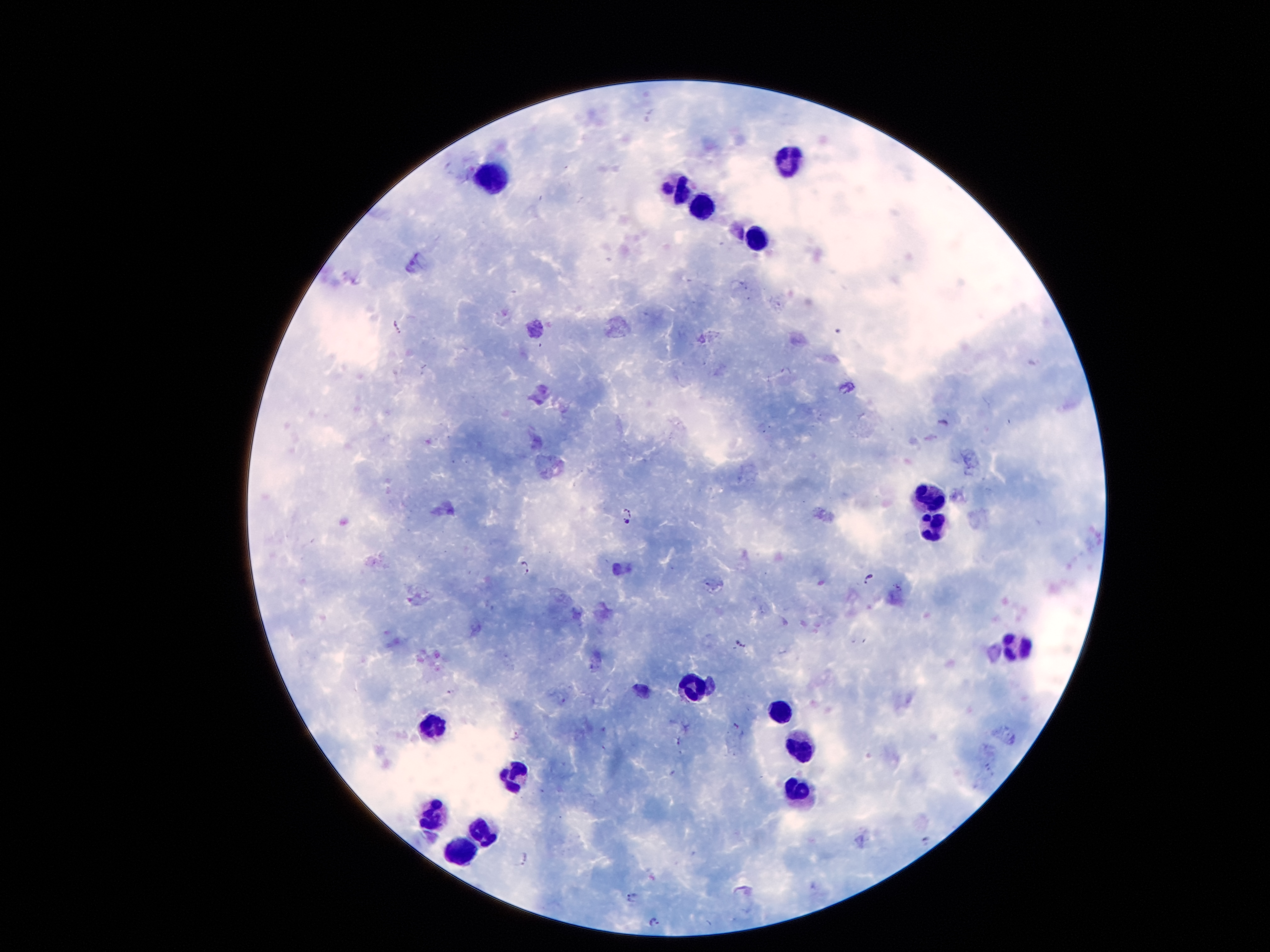
Approximate centers as [x, y] in pixels.
Summary:
  - Leukocyte locations: [787, 161], [495, 171], [685, 197], [703, 208], [751, 237], [928, 500], [928, 527], [1015, 648], [694, 692], [782, 716], [431, 735], [798, 748], [515, 774], [793, 794], [437, 819], [479, 830], [462, 852]
  - Plasmodium parasite locations: [399, 327], [943, 423], [627, 510], [626, 522], [527, 566], [869, 579], [742, 643], [735, 726], [927, 842], [522, 859], [632, 897], [654, 922]
  - Capture: smartphone through the microscope eyepiece
  - Image size: 1270×952 pixels
  - Field of view: single
  - Patient malaria status: positive for Plasmodium falciparum
  - Magnification: 100x
  - Preparation: thick blood film
  - Stain: Giemsa